Locate every blood parasite and identify its species.
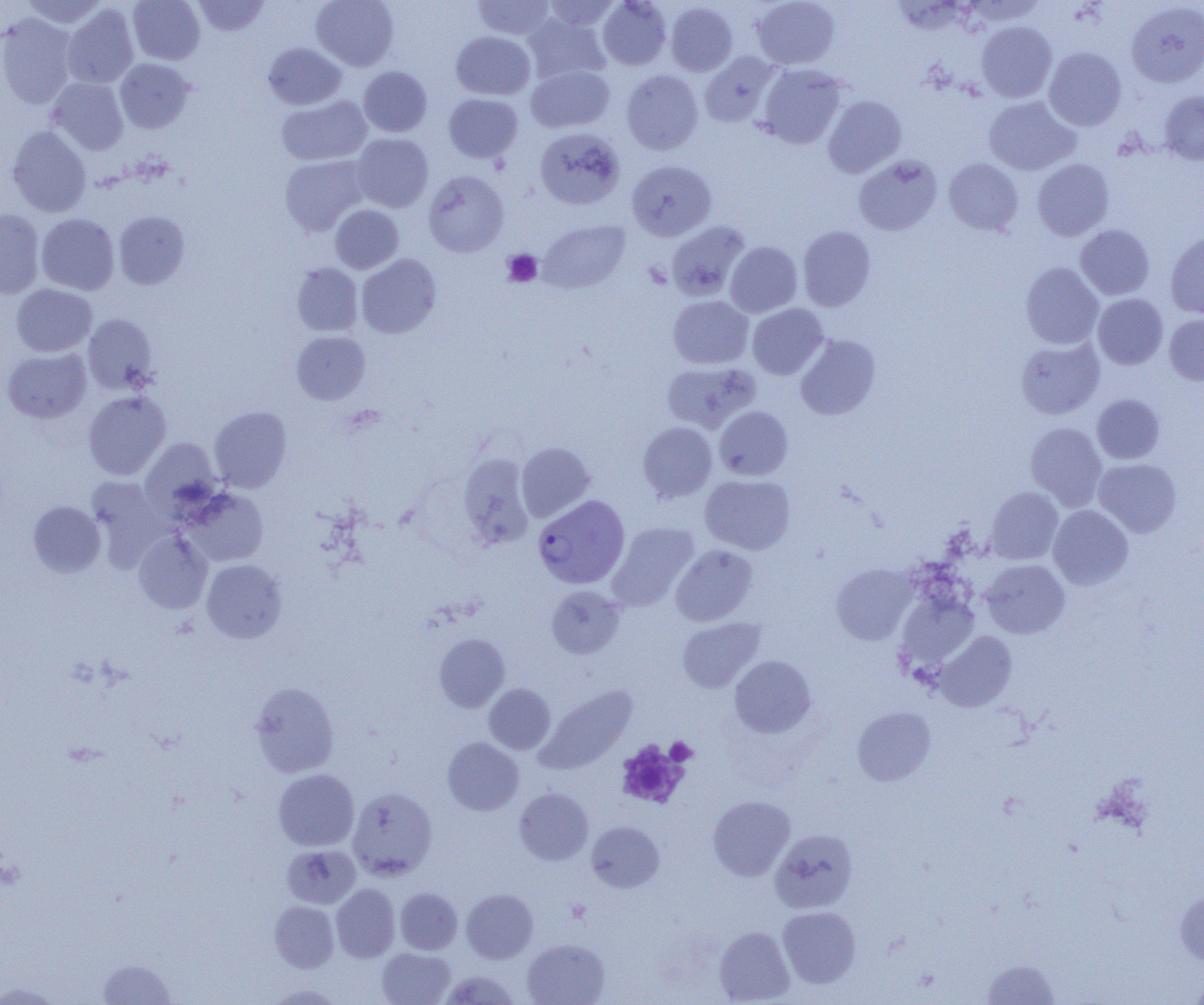
Approximate bounding boxes as (x1, y1, x2, y2) in pixels.
Plasmodium vivax-infected red blood cells: (533, 494, 630, 589).
No Plasmodium falciparum, Plasmodium ovale, Plasmodium malariae, Babesia divergens, or Trypanosoma brucei observed.

Summary:
  - Platelet locations: (502, 249, 542, 287), (665, 737, 697, 765), (616, 740, 688, 808)
  - Uninfected red blood cell locations: (20, 0, 108, 28), (128, 0, 205, 64), (192, 0, 270, 36), (311, 0, 399, 71), (473, 0, 555, 40), (541, 0, 621, 31), (597, 0, 672, 70), (751, 0, 840, 70), (665, 2, 738, 76), (1126, 2, 1204, 87), (62, 4, 138, 88), (0, 13, 77, 108), (524, 13, 610, 83), (976, 21, 1057, 102), (451, 31, 535, 100), (263, 43, 347, 109), (1044, 47, 1126, 131), (699, 51, 779, 127), (115, 58, 195, 133), (526, 64, 614, 133), (756, 64, 847, 149), (358, 66, 432, 137), (621, 70, 703, 155), (47, 78, 129, 154), (1159, 91, 1204, 165), (444, 93, 523, 163), (276, 95, 372, 166), (823, 95, 907, 177), (984, 96, 1079, 175), (7, 125, 91, 217), (535, 127, 625, 210), (351, 133, 434, 212), (279, 155, 369, 236), (854, 156, 942, 236), (944, 158, 1023, 235), (1032, 159, 1114, 241), (626, 160, 716, 240), (424, 170, 509, 257), (330, 204, 403, 273), (0, 209, 44, 298), (113, 211, 190, 289), (36, 214, 119, 295), (539, 220, 629, 293), (666, 221, 750, 301), (1075, 224, 1155, 300), (798, 226, 876, 311), (1166, 232, 1204, 319), (725, 241, 802, 317), (356, 254, 441, 339), (292, 262, 363, 336), (1021, 262, 1103, 349), (11, 284, 97, 356), (1092, 293, 1168, 369), (668, 295, 754, 369), (747, 304, 829, 379), (83, 314, 158, 394), (1164, 314, 1204, 385), (292, 331, 370, 404), (795, 334, 880, 420), (1015, 337, 1105, 419), (1, 347, 92, 423), (661, 362, 760, 433), (83, 391, 171, 480), (1092, 395, 1164, 464), (209, 406, 292, 492), (715, 406, 793, 480), (638, 422, 717, 503), (1025, 422, 1107, 509), (140, 437, 222, 517), (516, 442, 595, 522), (457, 453, 535, 549), (1093, 458, 1181, 537), (700, 474, 795, 555), (86, 477, 170, 565), (183, 487, 268, 566), (985, 487, 1063, 564), (28, 501, 105, 577), (1048, 505, 1133, 589), (607, 521, 699, 610), (133, 531, 212, 614), (671, 545, 758, 626), (201, 559, 287, 643), (981, 559, 1070, 638), (832, 563, 917, 645), (546, 585, 625, 659), (895, 591, 979, 677), (677, 617, 765, 693), (934, 631, 1017, 712), (434, 633, 510, 712), (730, 655, 816, 737), (249, 682, 339, 777), (484, 683, 555, 754), (535, 685, 638, 774), (852, 707, 936, 786), (442, 737, 524, 815), (274, 769, 359, 851), (347, 787, 438, 879), (515, 787, 593, 865), (708, 796, 795, 881), (587, 821, 664, 893), (770, 829, 858, 913), (281, 844, 361, 909), (331, 883, 400, 962), (1175, 887, 1204, 965), (395, 888, 462, 954), (461, 889, 538, 963), (269, 901, 339, 972), (777, 906, 862, 988), (714, 926, 795, 1004), (522, 939, 610, 1005), (377, 948, 455, 1005), (98, 958, 175, 1004), (982, 958, 1060, 1004), (438, 971, 522, 1004), (1189, 972, 1204, 1004), (0, 982, 61, 1004), (264, 984, 343, 1004)
  - Slide-level diagnosis: Plasmodium vivax
  - Magnification: 1000x
  - Field of view: single
  - Modality: optical microscopy
  - Preparation: thin blood smear
  - Image size: 1204×1005 pixels